Assess the morphology of the red blood cells.
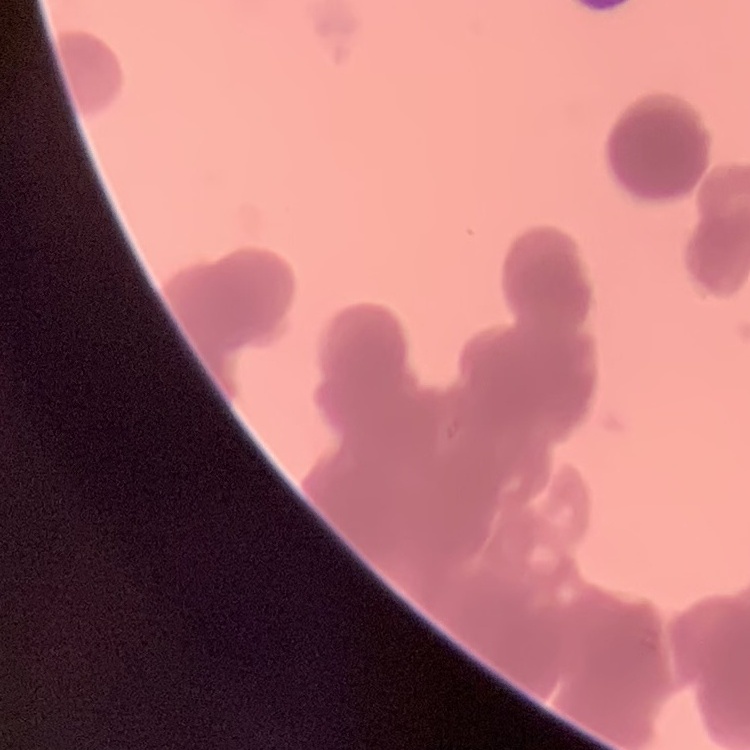
They show rouleaux formation.

Thin peripheral smear. Stained with either Field's or Giemsa. One tile cut from a larger photomicrograph.